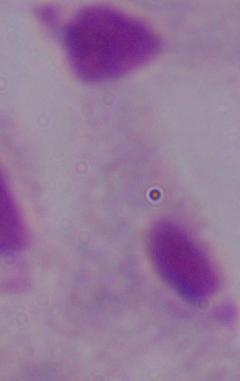

modality: micrograph
magnification: 1000x
identification: trichomonad